Classify this cell by malaria status.
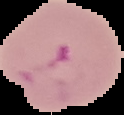
Parasitized.

image type = cell region segmented out of the field of view; surrounding area masked to black
preparation = thin blood film
image size = 124×115 pixels